Assess this cell for malaria.
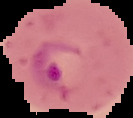

Parasitized.

Image is 133×118 pixels. From a thin blood film. Segmented cell region on a black background.